Locate every Plasmodium falciparum-infected red blood cell.
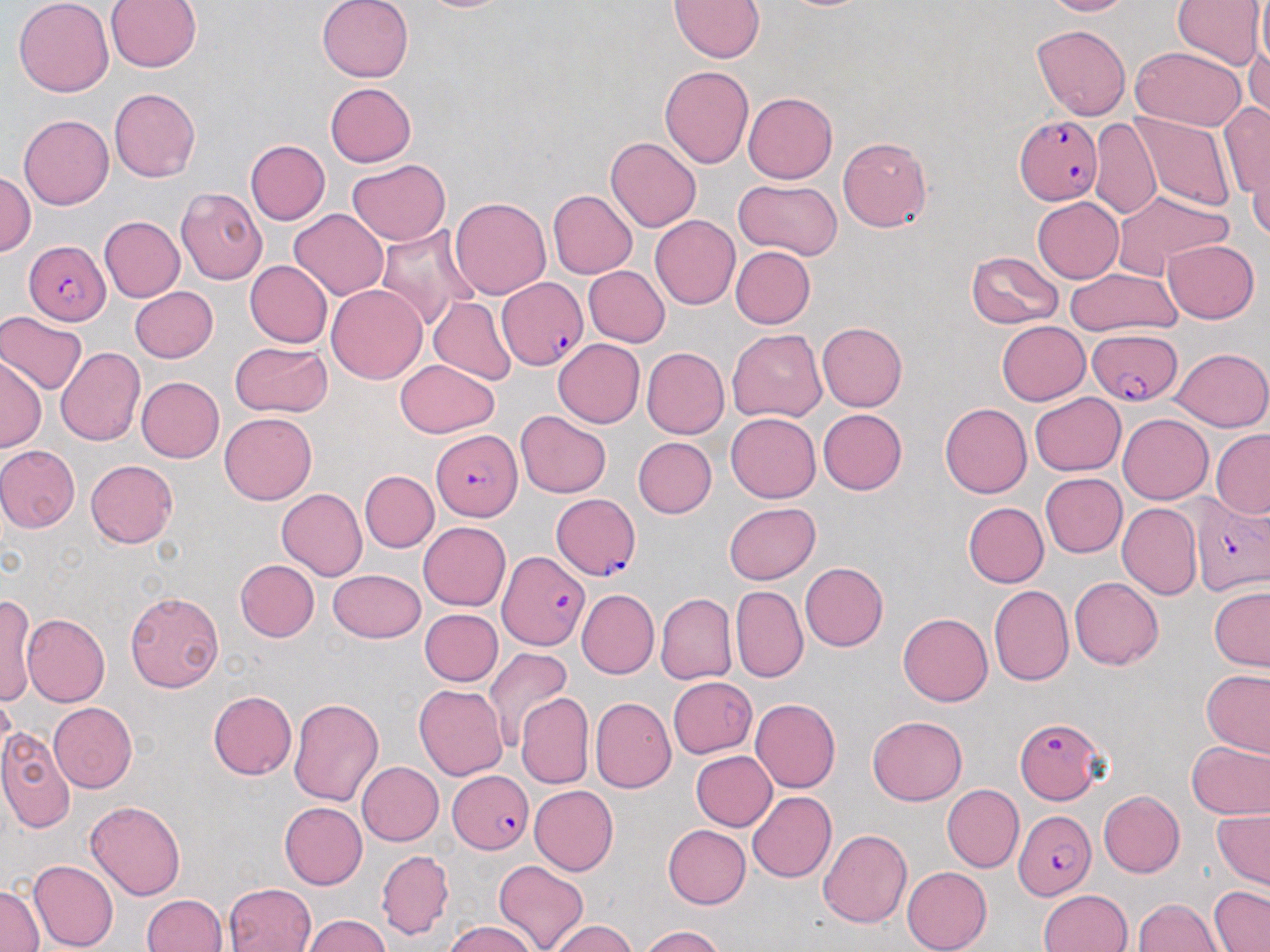
Approximate bounding boxes as [x1, y1, x2, y2] in pixels.
Plasmodium falciparum-infected red blood cells: [1014, 115, 1103, 205], [25, 240, 110, 324], [498, 278, 587, 371], [1085, 330, 1182, 406], [431, 428, 523, 522], [552, 492, 640, 579], [1189, 497, 1269, 596], [497, 551, 588, 650], [1016, 715, 1107, 804], [448, 770, 531, 854], [1014, 810, 1095, 900].

Summary:
  - Uninfected red blood cell locations: [13, 0, 114, 97], [317, 0, 414, 82], [413, 0, 517, 12], [670, 0, 765, 62], [1040, 0, 1134, 17], [1173, 0, 1266, 69], [106, 1, 201, 71], [1256, 1, 1270, 75], [1032, 24, 1130, 121], [1246, 37, 1270, 126], [1131, 47, 1246, 131], [660, 66, 754, 168], [324, 82, 415, 166], [109, 87, 201, 183], [742, 92, 837, 184], [1219, 100, 1270, 205], [1129, 111, 1235, 213], [19, 114, 113, 210], [1089, 118, 1161, 219], [837, 136, 933, 233], [605, 137, 702, 232], [245, 140, 330, 224], [1246, 140, 1270, 243], [346, 158, 450, 246], [1, 169, 35, 256], [734, 179, 841, 258], [175, 187, 267, 284], [547, 189, 637, 279], [1112, 189, 1232, 275], [450, 197, 551, 299], [1032, 197, 1123, 282], [289, 209, 389, 301], [649, 215, 740, 310], [99, 216, 185, 302], [375, 225, 477, 331], [1163, 239, 1259, 323], [731, 247, 815, 329], [966, 250, 1063, 329], [245, 261, 333, 347], [583, 265, 670, 347], [1065, 268, 1181, 336], [326, 284, 427, 384], [130, 286, 218, 362], [429, 297, 517, 385], [0, 310, 87, 395], [817, 321, 906, 411], [997, 321, 1091, 405], [5, 322, 138, 418], [727, 329, 827, 423], [553, 338, 645, 429], [229, 341, 331, 415], [57, 347, 145, 446], [642, 347, 729, 438], [1170, 347, 1269, 431], [0, 356, 45, 452], [395, 359, 498, 437], [136, 376, 224, 462], [1028, 393, 1125, 476], [940, 402, 1032, 498], [817, 408, 907, 495], [515, 410, 611, 498], [219, 412, 317, 504], [726, 413, 821, 502], [1117, 413, 1213, 504], [1211, 429, 1270, 518], [632, 437, 717, 517], [0, 445, 80, 532], [85, 460, 178, 548], [360, 470, 439, 551], [1040, 473, 1127, 557], [276, 489, 367, 580], [723, 502, 821, 584], [963, 502, 1049, 587], [1117, 503, 1202, 600], [419, 522, 511, 611], [235, 559, 319, 641], [800, 562, 888, 652], [328, 568, 425, 643], [1070, 578, 1162, 669], [988, 584, 1074, 685], [731, 585, 808, 683], [1209, 586, 1270, 671], [576, 589, 659, 679], [125, 590, 224, 693], [1, 592, 37, 708], [655, 592, 737, 685], [419, 609, 503, 686], [899, 612, 992, 706], [22, 614, 110, 707], [484, 645, 573, 749], [1202, 670, 1270, 756], [669, 677, 756, 758], [414, 684, 508, 780], [0, 691, 16, 767], [209, 691, 297, 779], [516, 693, 593, 789], [288, 697, 385, 806], [590, 697, 676, 793], [750, 698, 841, 792], [49, 702, 136, 792], [867, 715, 967, 805], [0, 728, 75, 834], [1186, 738, 1270, 820], [690, 750, 777, 830], [357, 761, 443, 845], [941, 783, 1023, 873], [530, 785, 618, 876], [748, 791, 836, 883], [1098, 791, 1185, 877], [86, 800, 186, 900], [279, 802, 367, 889], [1212, 809, 1269, 890], [663, 824, 750, 909], [818, 829, 912, 927], [376, 851, 454, 939], [27, 859, 119, 952], [494, 860, 589, 952], [902, 866, 992, 952], [224, 882, 317, 952], [1, 883, 43, 951], [1209, 886, 1269, 951], [1039, 889, 1132, 952], [142, 894, 228, 952], [1133, 897, 1222, 951], [303, 915, 391, 952], [445, 920, 538, 952], [548, 920, 638, 952], [640, 926, 725, 952]
  - Slide-level diagnosis: Plasmodium falciparum
  - Stain: May-Grünwald-Giemsa
  - Preparation: thin blood film
  - Modality: optical microscopy
  - Image size: 1270×952 pixels
  - Magnification: 1000x
  - Field of view: one of a larger specimen